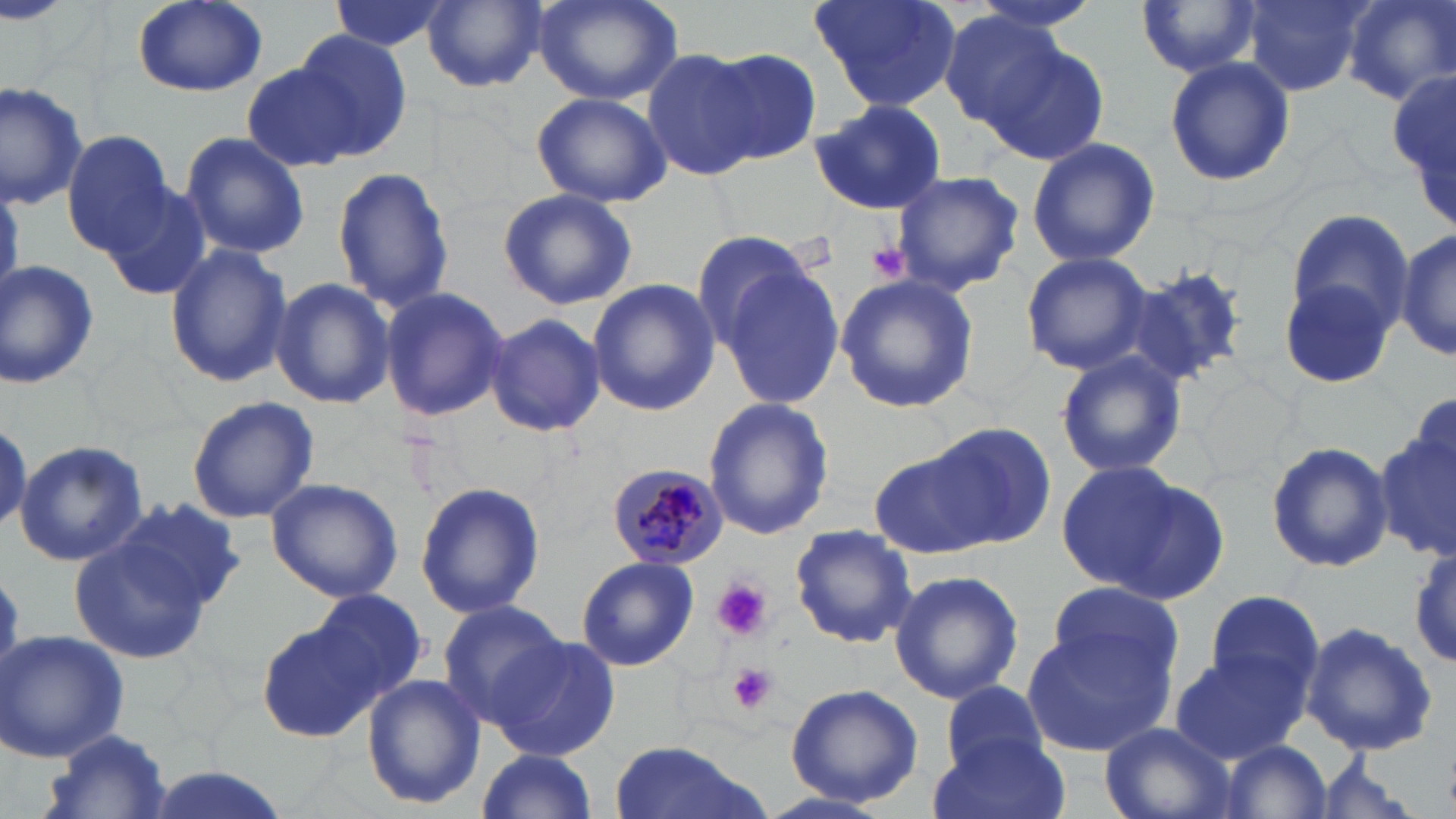 Approximate bounding boxes as [x1, y1, x2, y2] in pixels. Plasmodium malariae-infected red blood cell locations: [606, 462, 727, 569]. Uninfected red blood cell locations: [130, 0, 268, 97], [325, 0, 450, 54], [422, 0, 547, 91], [534, 0, 682, 106], [809, 0, 961, 112], [959, 0, 1111, 34], [1345, 0, 1456, 106], [1134, 1, 1260, 80], [1243, 1, 1367, 96], [938, 10, 1070, 131], [290, 30, 411, 158], [978, 36, 1108, 164], [641, 48, 769, 181], [705, 48, 823, 168], [1165, 55, 1294, 188], [240, 62, 362, 173], [1390, 62, 1456, 226], [0, 79, 92, 212], [533, 92, 670, 208], [811, 100, 948, 216], [62, 131, 176, 254], [181, 131, 309, 259], [1025, 135, 1160, 267], [329, 165, 455, 313], [892, 171, 1024, 293], [101, 178, 212, 303], [498, 189, 638, 311], [1281, 208, 1413, 347], [688, 228, 816, 352], [1397, 229, 1454, 362], [163, 241, 294, 388], [1020, 251, 1153, 375], [0, 259, 101, 390], [1125, 262, 1249, 386], [720, 265, 844, 410], [1278, 268, 1401, 392], [836, 272, 980, 414], [269, 278, 394, 409], [586, 279, 719, 416], [378, 286, 511, 423], [482, 313, 606, 436], [1055, 349, 1186, 482], [187, 394, 319, 523], [702, 397, 835, 542], [924, 420, 1057, 547], [1375, 427, 1453, 561], [1265, 440, 1394, 577], [15, 441, 148, 567], [867, 443, 1007, 560], [1059, 465, 1220, 600], [266, 479, 403, 603], [414, 481, 546, 620], [81, 502, 243, 651], [788, 525, 919, 649], [1410, 537, 1455, 673], [576, 556, 699, 672], [887, 569, 1024, 704], [1046, 583, 1186, 698], [310, 587, 430, 703], [1203, 589, 1325, 709], [436, 600, 568, 726], [255, 616, 381, 745], [1302, 620, 1439, 759], [1023, 621, 1174, 755], [0, 630, 130, 760], [485, 636, 622, 762], [1170, 652, 1309, 764], [363, 675, 486, 810], [937, 679, 1049, 777], [783, 682, 924, 807], [1099, 722, 1238, 819], [42, 731, 175, 819], [931, 731, 1071, 819], [604, 739, 765, 819], [1219, 739, 1335, 818], [475, 749, 599, 819], [1297, 758, 1426, 819]. Platelet locations: [867, 241, 912, 285], [713, 580, 772, 641], [727, 663, 776, 715]. Slide-level diagnosis: Plasmodium malariae. Light microscopy. Single field of view. Thin blood smear. May-Grünwald-Giemsa-stained preparation. 1000x magnification. Image is 1456×819 pixels.